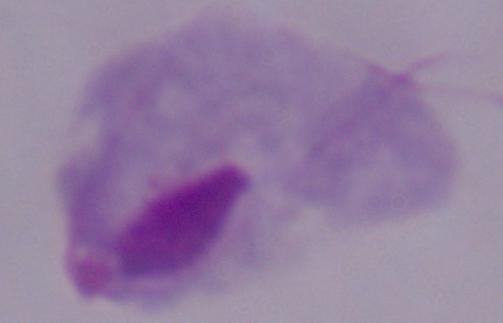
magnification = 1000x
identification = trichomonad
modality = micrograph